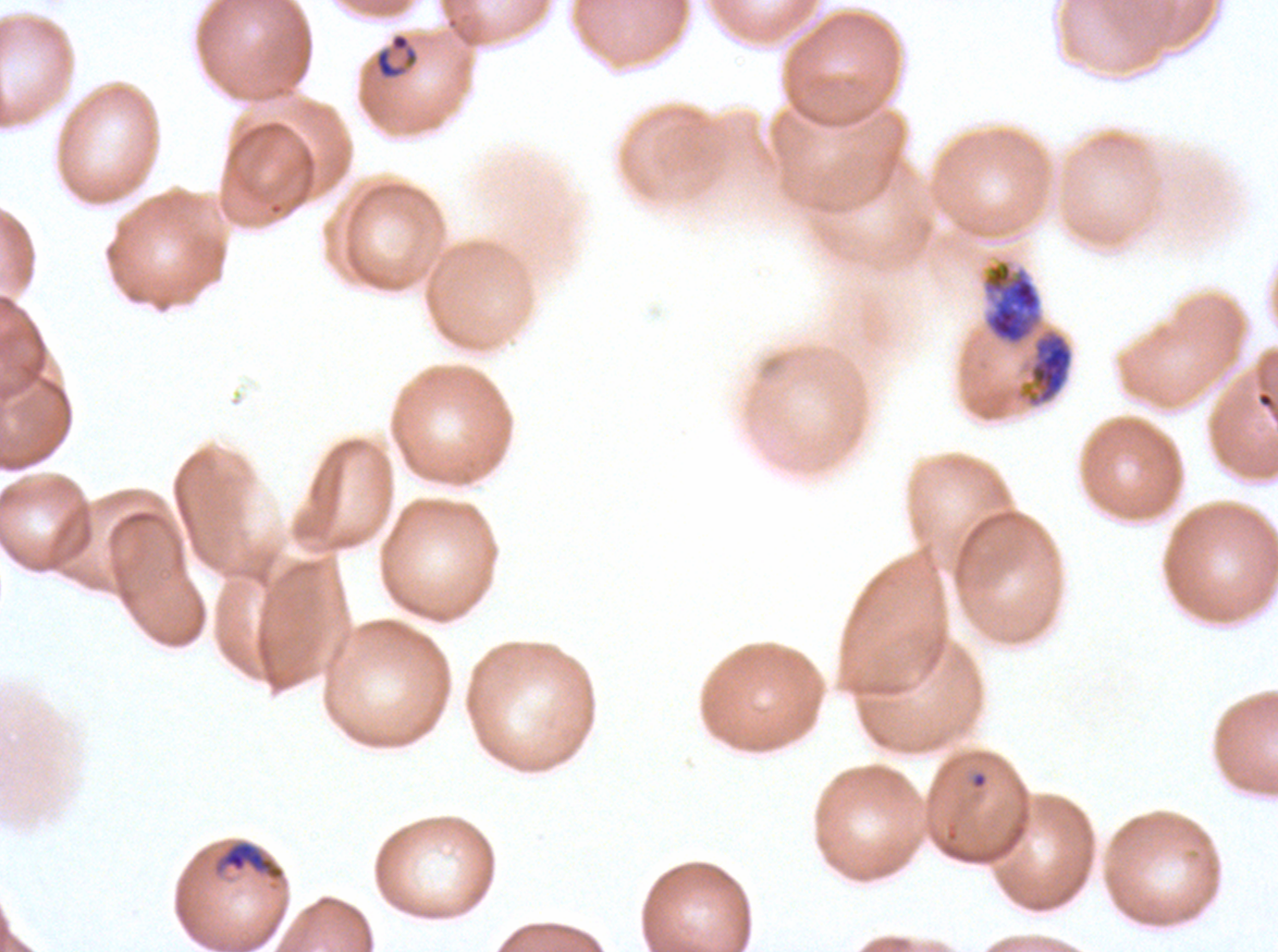
Approximate bounding rectangles given as corner coordinates in pixels from the top-left. Early schizont locations: (x1=982, y1=260, x2=1042, y2=346). Ring locations: (x1=374, y1=31, x2=419, y2=80), (x1=969, y1=770, x2=989, y2=790). Mid trophozoite locations: (x1=221, y1=841, x2=283, y2=878). Late trophozoite locations: (x1=1021, y1=329, x2=1074, y2=408). Image is 1278×952 pixels. P. falciparum from a patient in The Gambia, cultured ex vivo for 24 to 48 hours. Life-cycle stages observed: ring, mid trophozoite, late trophozoite, early schizont. A sub-image separated from a larger composite. Thin blood smear. Giemsa-stained preparation.